Locate every malaria parasite.
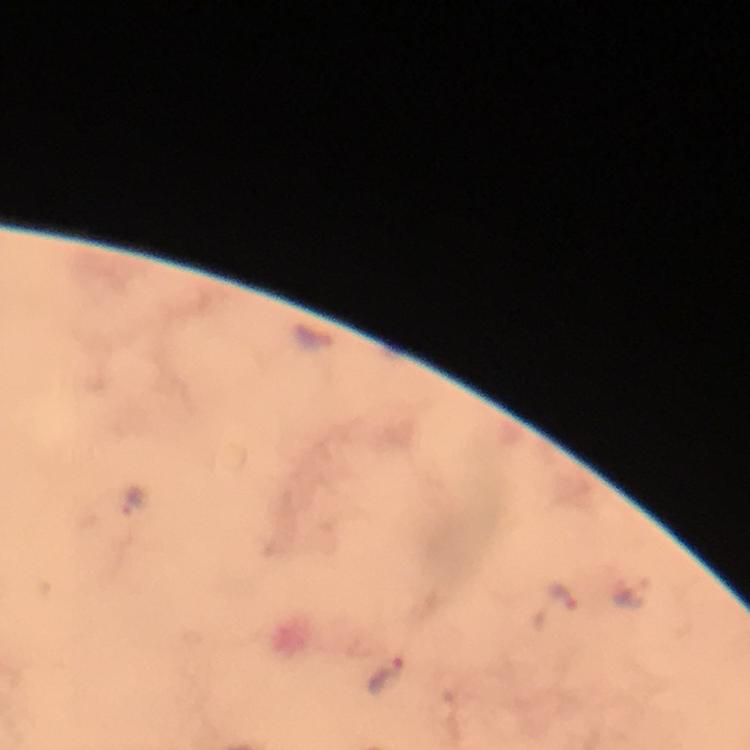

Approximate object centers, in pixels from the top-left corner.
Malaria parasites: (x=136, y=502), (x=549, y=604), (x=385, y=674).

Summary:
  - Magnification: 100x
  - Image size: 750×750 pixels
  - Immersion oil: used
  - Context: from a malaria diagnostic workup
  - Preparation: thick blood smear
  - Cropped from: one field of view
  - Stain: Giemsa
  - Capture: smartphone mounted on the microscope